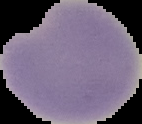
Summary:
  - Image type: segmented cell region on a black background
  - Result: Plasmodium parasites detected
  - Image size: 142×124 pixels
  - Preparation: thin blood film